Report the malaria status of this cell.
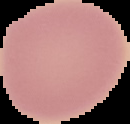
It is uninfected.

The area outside the segmented cell region is set to black. Image is 130×124 pixels. From a thin blood smear.